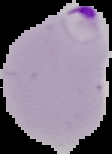
malaria status = parasitized
image size = 112×154 pixels
image type = segmented cell region with the area outside set to black
preparation = thin blood film